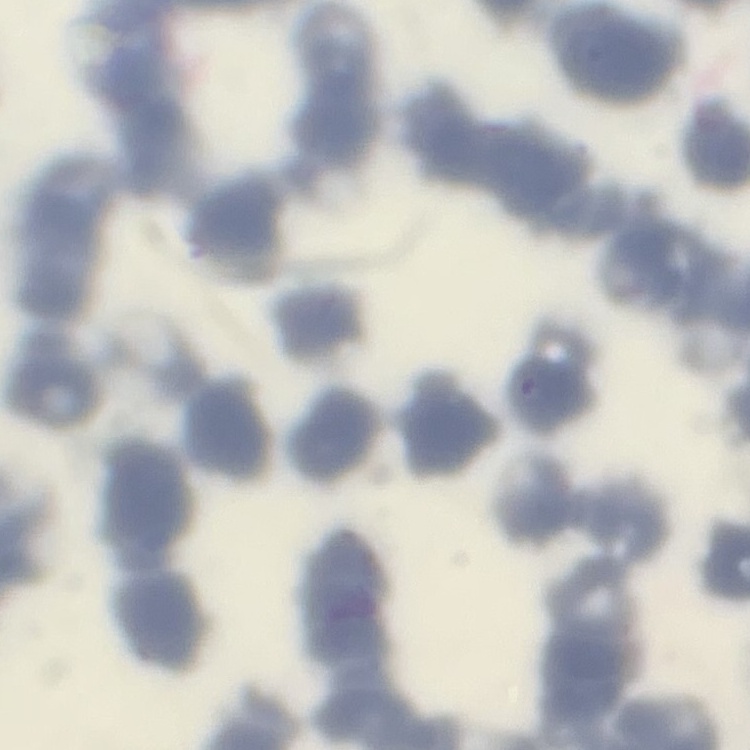

erythrocyte morphology = rouleaux formation
preparation = thin blood film
stain = Field's or Giemsa
image type = square crop of a larger photomicrograph